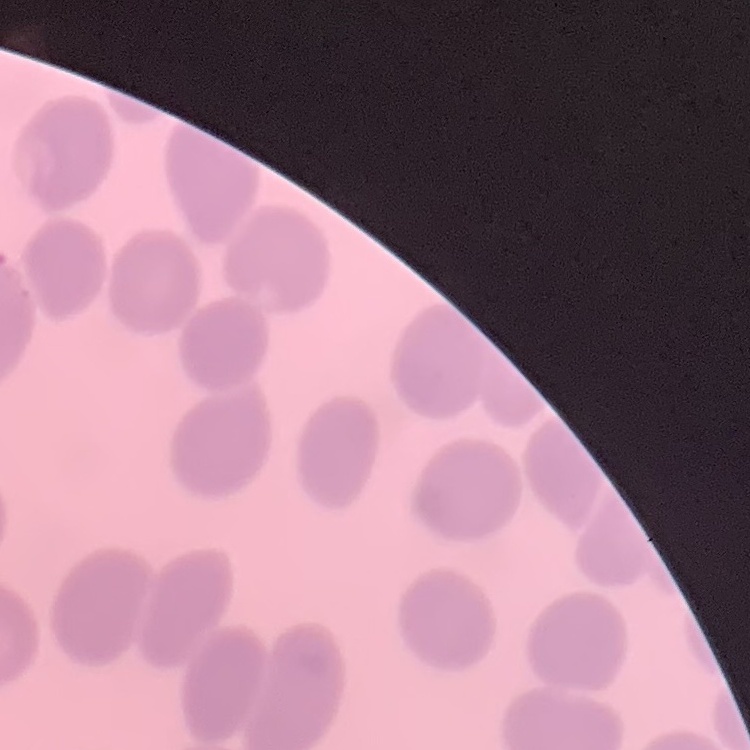

{
  "erythrocyte_morphology": "no rouleaux formation",
  "image_type": "square crop of a larger photomicrograph",
  "preparation": "thin peripheral smear",
  "stain": "Field's or Giemsa"
}